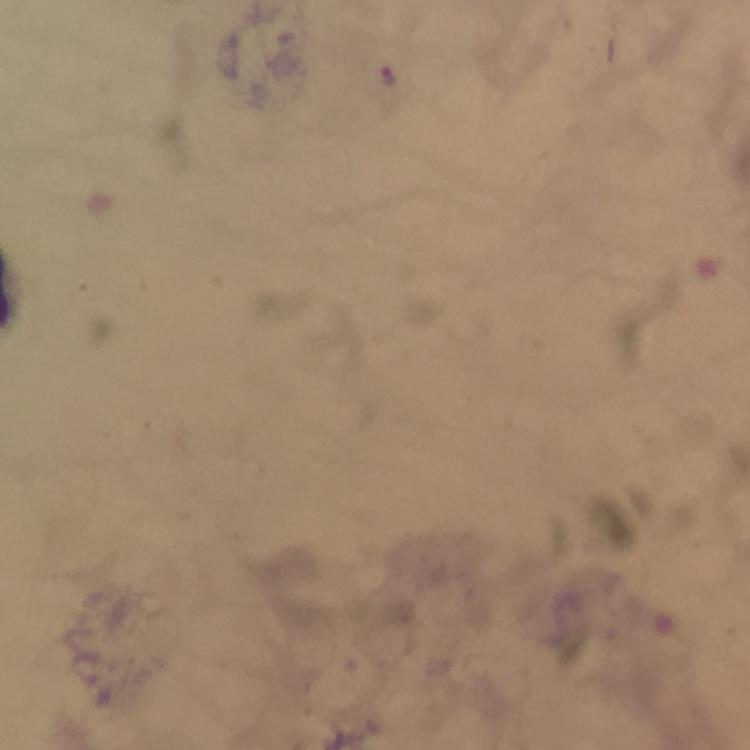

Approximate centers as [x, y] in pixels.
Summary:
  - Malaria parasite locations: [388, 75]
  - Immersion oil: used
  - Cropped from: one field of view
  - Stain: Giemsa
  - Context: from a malaria diagnostic workup
  - Magnification: 100x
  - Preparation: thick blood film
  - Capture: smartphone photograph through a microscope
  - Image size: 750×750 pixels